Locate every leukocyte (white blood cell).
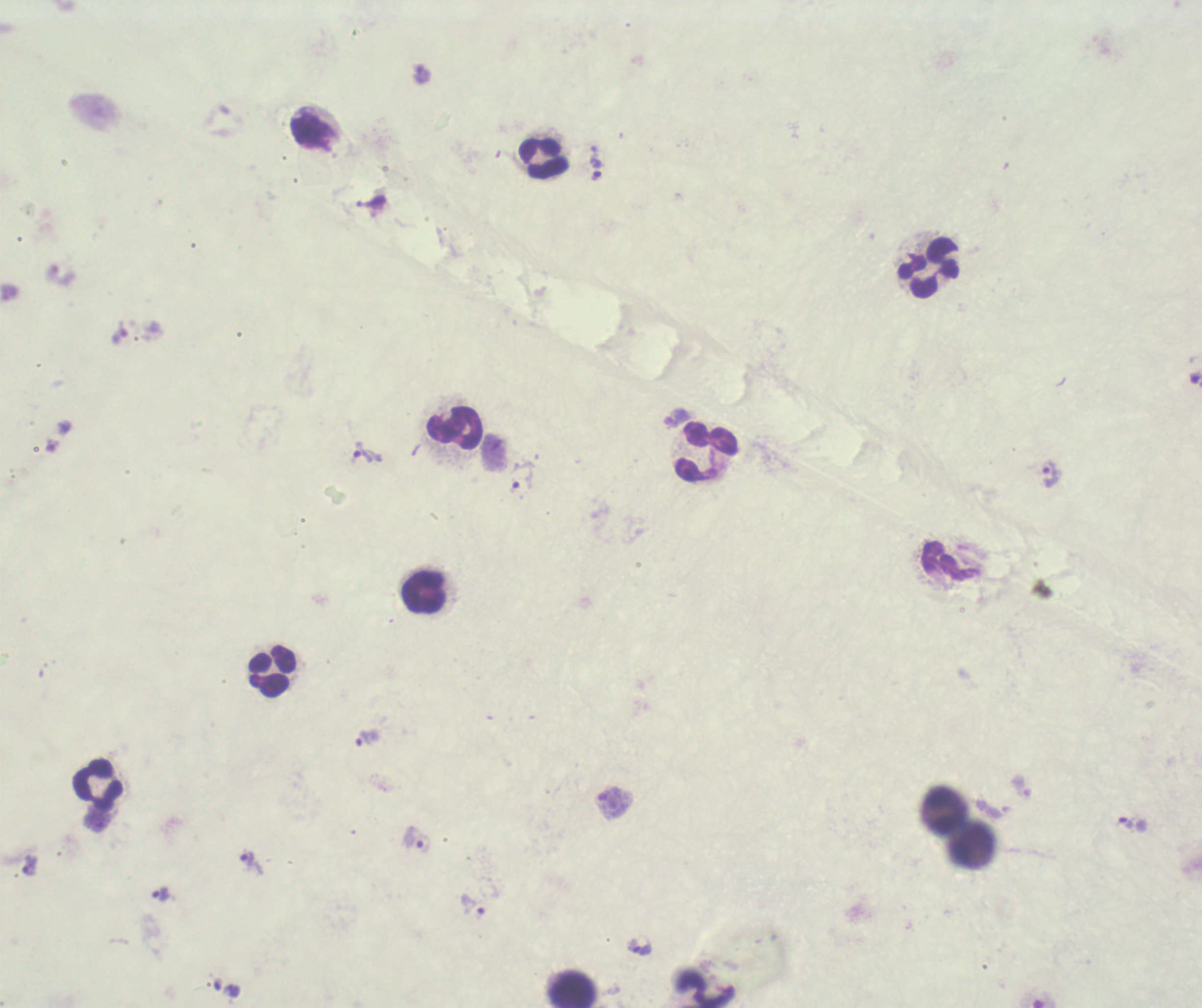

Approximate centers as {x, y} in pixels.
Leukocytes: {313, 133}, {544, 159}, {930, 268}, {454, 429}, {705, 453}, {945, 561}, {425, 593}, {272, 672}, {98, 785}, {944, 809}, {972, 848}, {573, 988}, {704, 988}.

{
  "image_size": "1202×1008 pixels",
  "magnification": "100x",
  "background_quality": "unsatisfactory",
  "stain": "Romanowsky",
  "result": "malaria parasites identified",
  "context": "previously used in a real diagnosis",
  "coloration_quality": "bad",
  "preparation": "thick smear of blood",
  "field_of_view": "single",
  "trophozoite_locations": "approximate centers as {x, y} in pixels: {597, 176}, {367, 452}, {1050, 474}, {522, 479}, {366, 737}, {415, 843}, {249, 862}, {30, 865}, {160, 894}, {473, 904}"
}